Assess this cell for malaria.
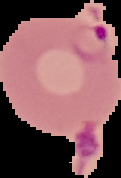
Parasitized.

From a thin blood film. Image is 121×178 pixels. The area outside the segmented cell region is set to black.